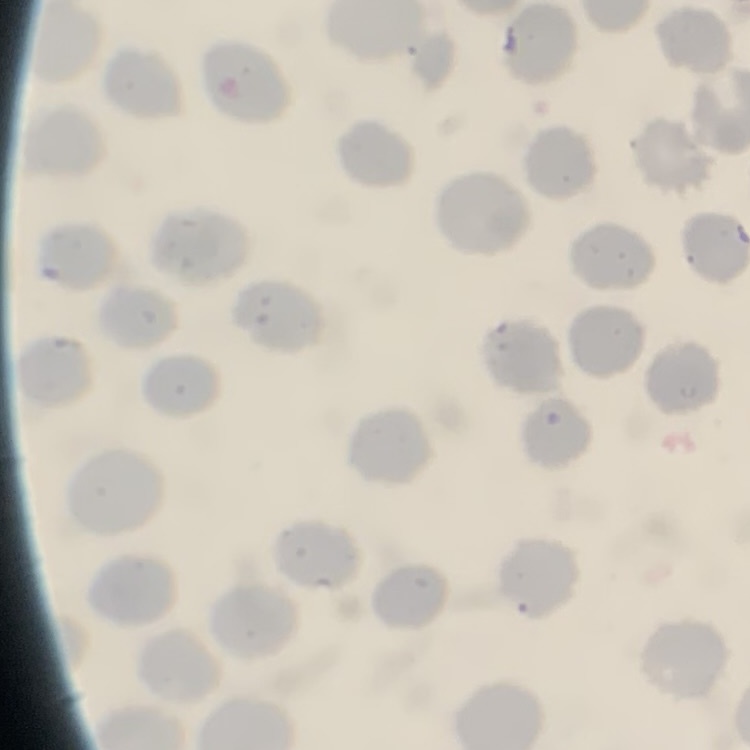
The red blood cells show no rouleaux formation. Thin blood smear. Field's or Giemsa stain. Square crop of a larger photomicrograph.